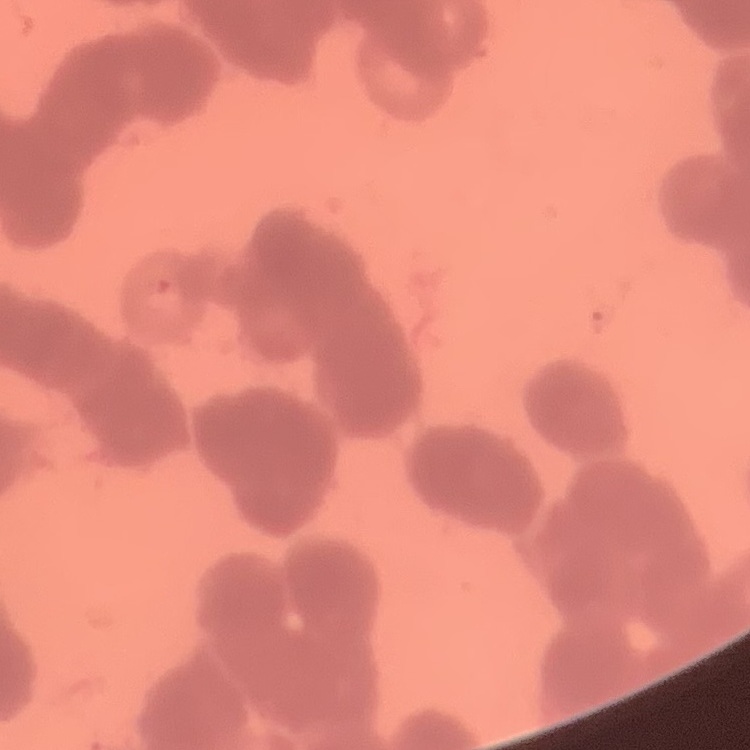

Summary:
  - Red blood cell morphology: rouleaux formation
  - Preparation: thin peripheral smear
  - Image type: one tile cut from a larger photomicrograph
  - Stain: Field's or Giemsa